Report the malaria status of this cell.
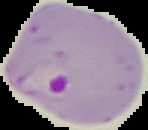
It is parasitized.

image size = 148×130 pixels
image type = cell region segmented out of the field of view; surrounding area masked to black
preparation = thin blood smear